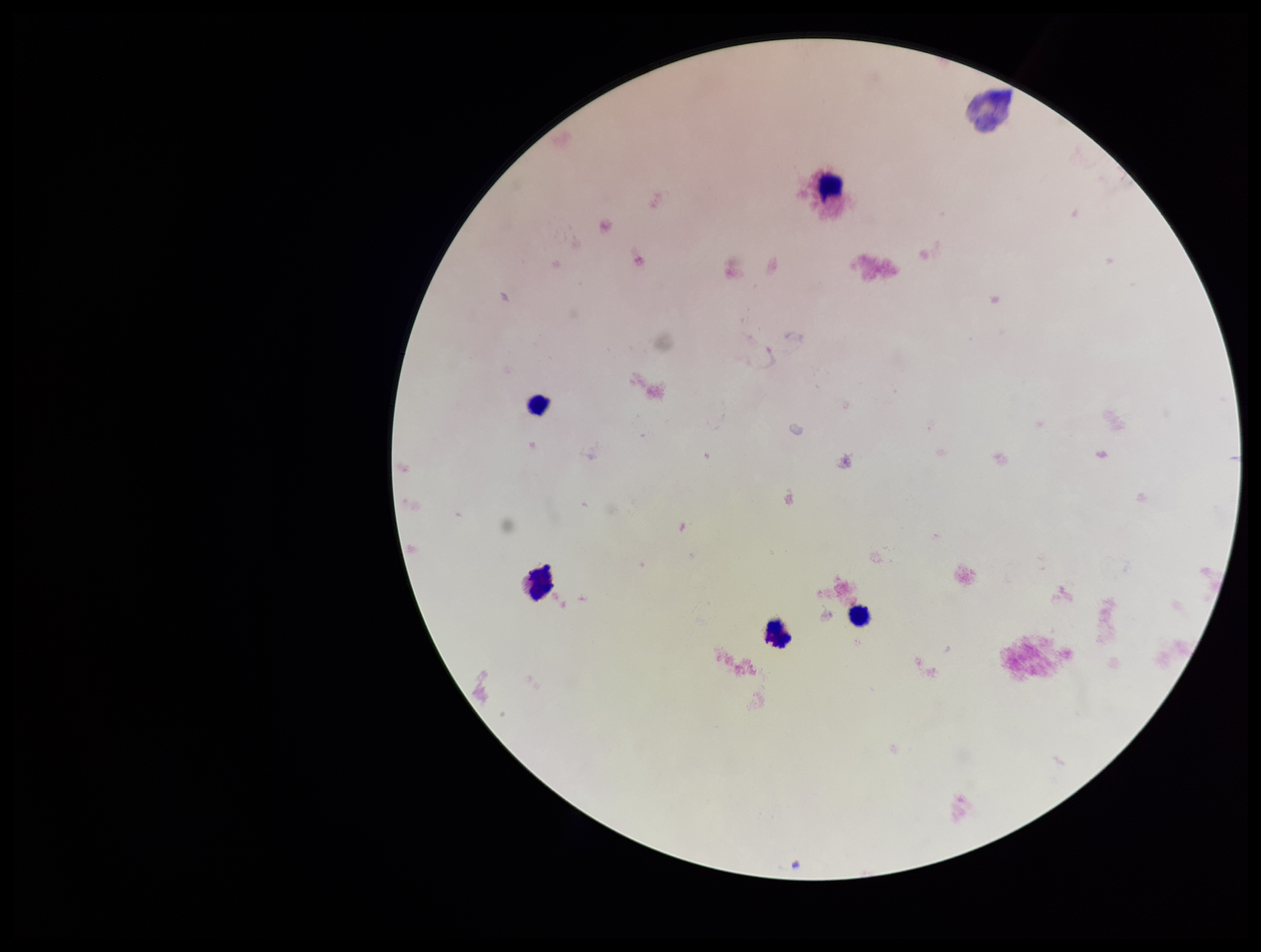

Summary:
  - Capture: smartphone photograph through the microscope eyepiece
  - Preparation: thick
  - Plasmodium parasites: none seen
  - Field of view: single
  - Parasite count: 0
  - Image size: 1261×952 pixels
  - Patient malaria status: negative
  - Leukocyte count: 5
  - Stain: Giemsa